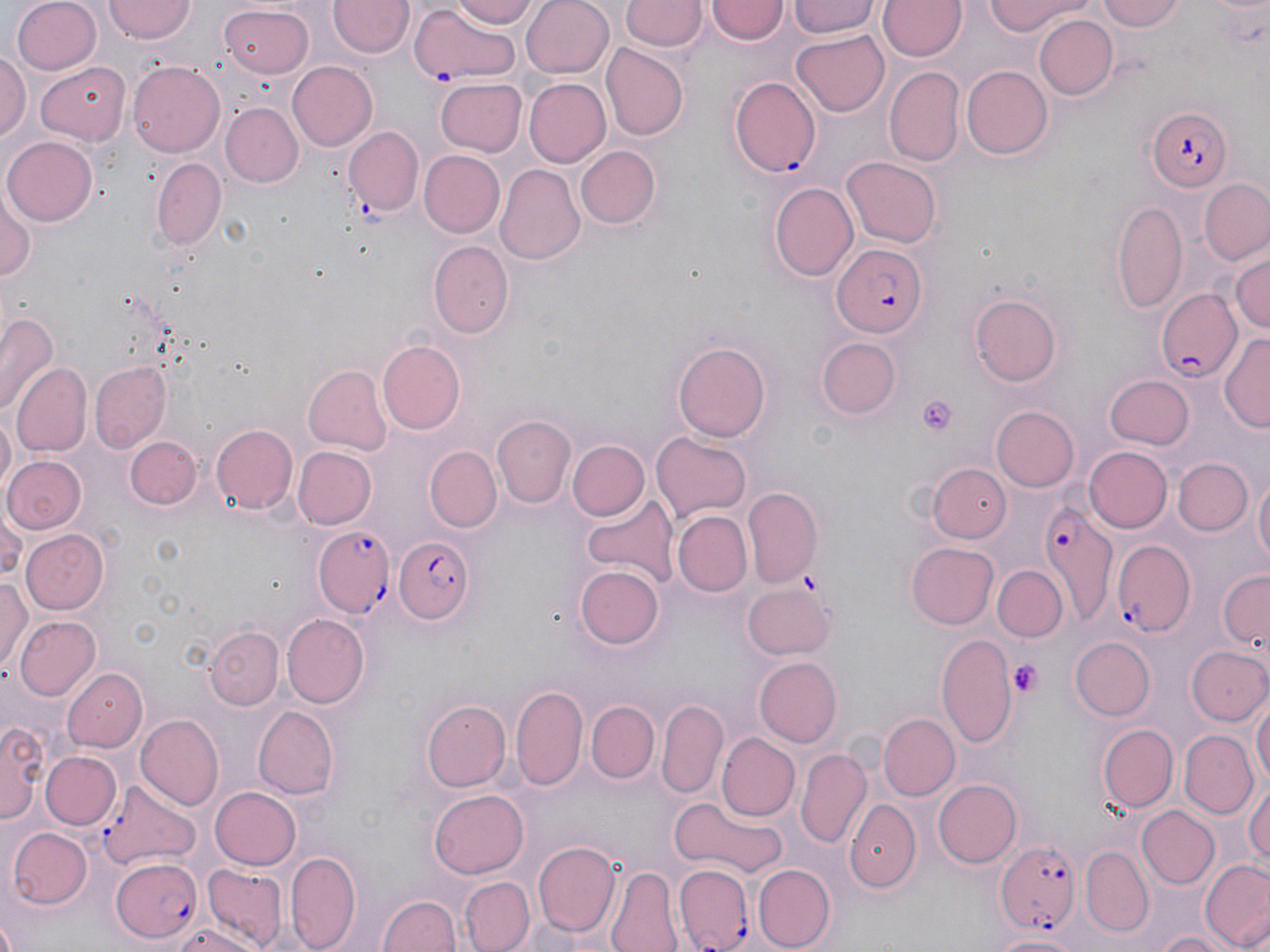
slide-level diagnosis = Plasmodium falciparum
platelet locations = approximate bounding boxes as [x1, y1, x2, y2] in pixels: [917, 395, 960, 436], [1008, 659, 1042, 697]
image size = 1270×952 pixels
uninfected red blood cell locations = approximate bounding boxes as [x1, y1, x2, y2] in pixels: [10, 0, 102, 74], [104, 0, 195, 42], [329, 0, 413, 59], [451, 0, 541, 28], [519, 0, 614, 76], [787, 0, 880, 39], [877, 0, 968, 62], [983, 0, 1093, 37], [1098, 0, 1185, 33], [621, 1, 705, 54], [707, 1, 789, 46], [218, 4, 314, 80], [1033, 14, 1117, 100], [790, 30, 891, 117], [601, 43, 687, 142], [0, 51, 30, 144], [127, 60, 225, 157], [286, 60, 378, 151], [35, 62, 130, 145], [961, 64, 1052, 158], [885, 66, 964, 166], [436, 77, 527, 155], [523, 78, 610, 167], [221, 103, 301, 186], [345, 126, 423, 216], [4, 134, 97, 225], [574, 145, 661, 228], [420, 150, 505, 236], [149, 156, 227, 250], [842, 157, 941, 248], [497, 163, 588, 265], [1199, 177, 1269, 267], [770, 181, 859, 283], [0, 184, 36, 290], [1112, 200, 1188, 314], [427, 241, 514, 337], [1229, 252, 1269, 338], [972, 292, 1065, 385], [0, 310, 58, 420], [1221, 331, 1270, 433], [817, 337, 902, 418], [376, 338, 466, 435], [673, 340, 771, 443], [88, 362, 172, 452], [12, 364, 91, 457], [302, 365, 391, 455], [1104, 375, 1193, 451], [992, 407, 1080, 490], [0, 410, 15, 499], [490, 414, 575, 508], [209, 423, 297, 515], [650, 430, 753, 520], [125, 434, 203, 510], [567, 440, 651, 522], [293, 447, 376, 529], [426, 447, 502, 532], [1084, 447, 1172, 533], [2, 455, 86, 537], [1173, 458, 1253, 536], [930, 463, 1012, 541], [1253, 474, 1269, 572], [743, 486, 823, 587], [580, 493, 677, 590], [0, 507, 24, 583], [673, 510, 752, 597], [21, 526, 110, 614], [907, 542, 998, 627], [577, 564, 663, 648], [994, 565, 1067, 643], [1217, 569, 1269, 653], [0, 576, 30, 671], [740, 582, 835, 660], [280, 614, 369, 708], [14, 615, 100, 703], [205, 627, 284, 709], [935, 632, 1018, 747], [1072, 637, 1156, 720], [1188, 646, 1269, 726], [754, 657, 842, 747], [63, 665, 145, 749], [513, 685, 587, 794], [422, 697, 511, 792], [1252, 697, 1269, 793], [587, 701, 660, 782], [656, 701, 728, 797], [252, 705, 339, 798], [877, 713, 959, 799], [137, 715, 224, 809], [2, 716, 47, 824], [1097, 723, 1178, 812], [1179, 730, 1256, 819], [717, 732, 799, 822], [797, 749, 872, 850], [43, 751, 120, 831], [932, 776, 1022, 866], [99, 778, 201, 869], [1247, 779, 1270, 872], [210, 786, 302, 871], [430, 788, 528, 879], [668, 798, 790, 880], [845, 798, 922, 896], [1138, 805, 1217, 889], [9, 827, 91, 909], [533, 841, 620, 937], [1080, 846, 1154, 937], [287, 849, 361, 952], [1200, 857, 1270, 950], [753, 863, 836, 949], [203, 864, 289, 947], [605, 867, 682, 952], [460, 875, 536, 952], [377, 891, 463, 952], [166, 924, 264, 952], [1151, 930, 1239, 952], [991, 932, 1080, 951]
Plasmodium falciparum-infected red blood cell locations = approximate bounding boxes as [x1, y1, x2, y2] in pixels: [407, 6, 524, 85], [730, 77, 820, 177], [1147, 105, 1231, 192], [834, 244, 926, 338], [1157, 288, 1242, 381], [1039, 500, 1120, 627], [311, 523, 395, 616], [391, 534, 476, 627], [1111, 539, 1195, 634], [995, 838, 1081, 936], [108, 855, 207, 943], [673, 864, 755, 949]
stain = May-Grünwald-Giemsa
modality = optical microscopy
magnification = 1000x
field of view = single
preparation = thin blood smear